Locate every uninfected red blood cell.
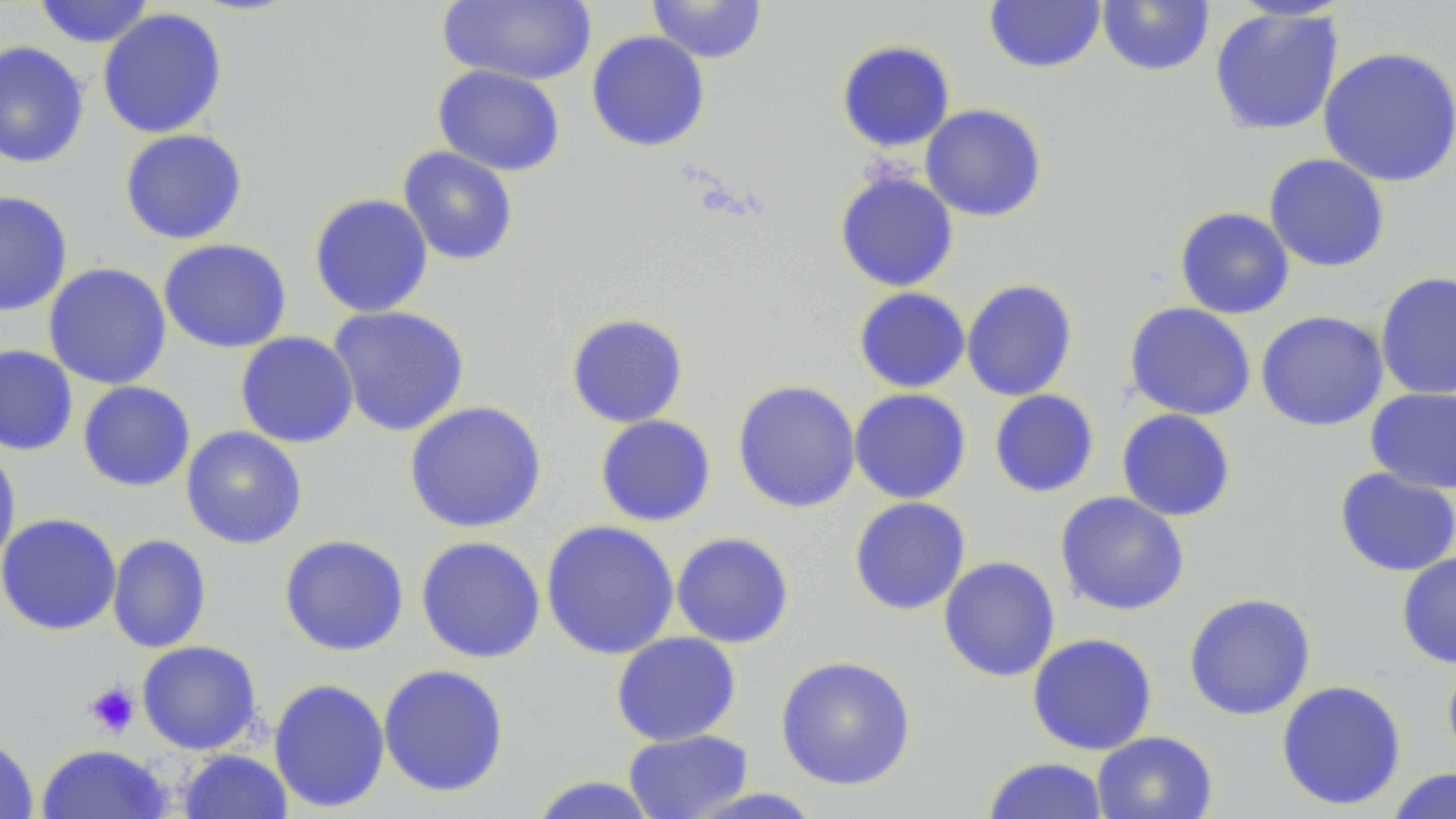

Approximate bounding boxes as (x1, y1, x2, y2) in pixels.
Uninfected red blood cells: (437, 0, 596, 86), (646, 0, 767, 64), (32, 1, 156, 48), (983, 1, 1106, 74), (1096, 1, 1215, 77), (1209, 6, 1345, 136), (97, 7, 228, 139), (586, 30, 711, 152), (835, 39, 956, 152), (0, 40, 90, 169), (1318, 46, 1456, 187), (432, 65, 566, 176), (920, 103, 1048, 222), (119, 129, 248, 245), (397, 145, 519, 266), (1263, 153, 1391, 273), (834, 170, 959, 292), (0, 190, 73, 316), (308, 193, 434, 318), (1175, 206, 1295, 319), (158, 238, 292, 353), (43, 262, 172, 390), (1375, 271, 1456, 401), (961, 278, 1078, 401), (853, 287, 970, 393), (1124, 302, 1256, 420), (327, 305, 470, 437), (1255, 310, 1389, 432), (565, 312, 689, 428), (234, 331, 359, 449), (0, 344, 78, 456), (732, 379, 861, 513), (77, 381, 196, 492), (1365, 387, 1456, 494), (849, 388, 972, 504), (988, 389, 1100, 498), (404, 401, 547, 533), (1116, 408, 1237, 522), (595, 414, 717, 527), (180, 426, 308, 549), (0, 444, 21, 576), (1334, 468, 1456, 577), (1054, 491, 1190, 616), (848, 497, 971, 615), (0, 513, 122, 636), (540, 520, 680, 661), (670, 531, 795, 648), (106, 534, 212, 654), (279, 534, 409, 657), (415, 536, 546, 664), (1396, 552, 1456, 669), (938, 556, 1061, 682), (1183, 592, 1317, 720), (611, 631, 742, 746), (1026, 632, 1158, 755), (136, 640, 262, 755), (775, 655, 917, 791), (1442, 659, 1456, 772), (377, 664, 510, 798), (268, 677, 391, 813), (1276, 679, 1407, 810), (623, 729, 754, 819), (1091, 730, 1218, 819), (0, 734, 39, 819), (35, 744, 174, 819), (176, 749, 293, 819), (981, 756, 1110, 818), (1386, 768, 1455, 819), (528, 775, 661, 819), (684, 787, 826, 818).

Summary:
  - Platelet locations: (83, 682, 140, 737)
  - Slide-level diagnosis: negative for blood parasites
  - Magnification: 1000x
  - Preparation: thin blood smear
  - Field of view: one of a larger specimen
  - Image size: 1456×819 pixels
  - Modality: optical microscopy
  - Stain: May-Grünwald-Giemsa